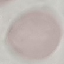
result: no malaria parasites detected
image_type: automatically extracted cell patch, resized to 64 × 64 pixels
stain: Giemsa
preparation: thin blood smear
capture: smartphone through the microscope eyepiece